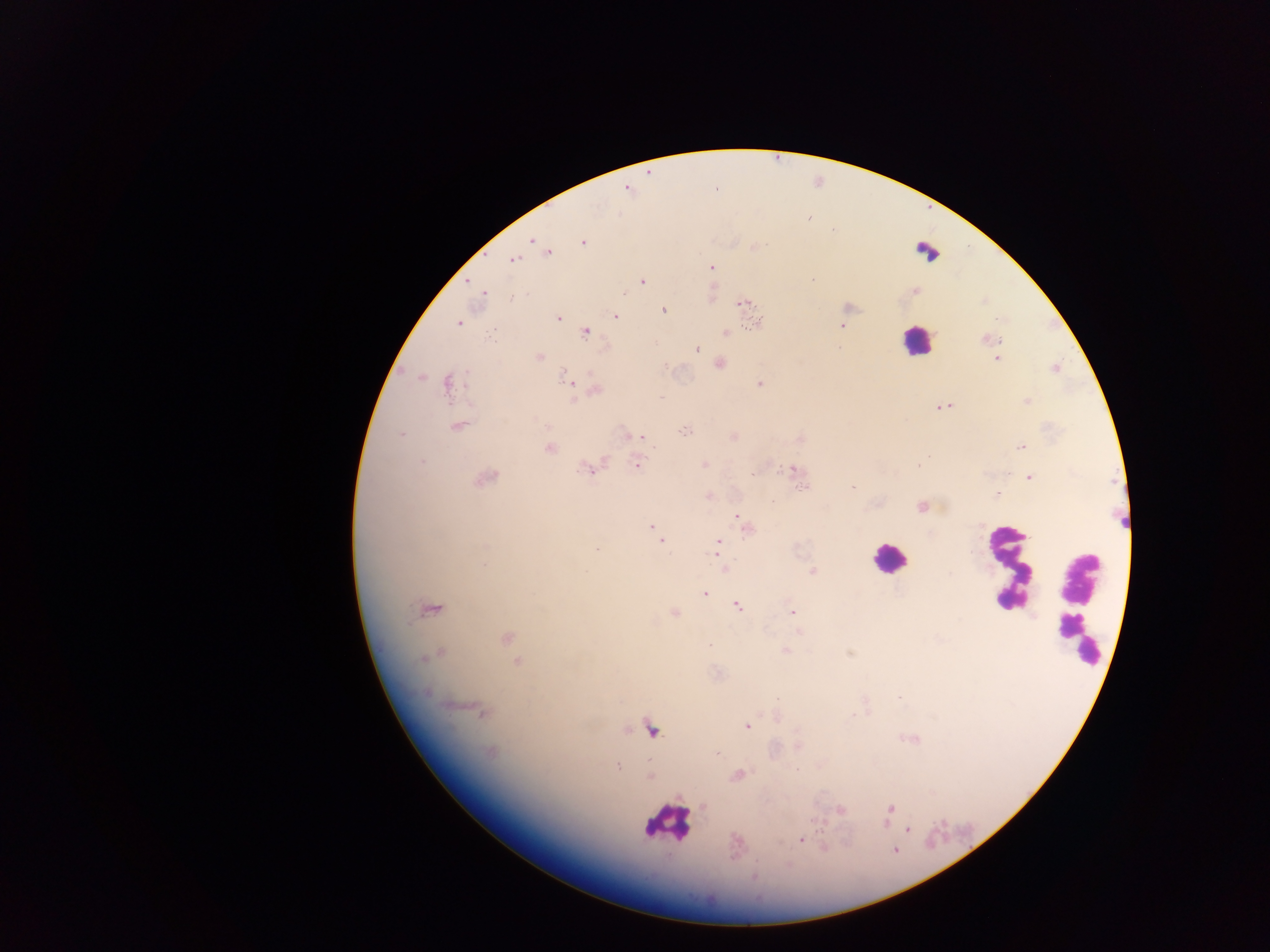

{
  "malaria_parasite_locations": "approximate centers as (x, y) in pixels: (627, 189), (808, 216), (533, 240), (583, 241), (548, 251), (513, 259), (711, 267), (813, 280), (641, 281), (467, 282), (915, 291), (483, 292), (710, 292), (512, 296), (743, 303), (747, 304), (662, 310), (615, 316), (558, 318), (458, 322), (757, 322), (842, 326), (585, 332), (725, 332), (987, 338), (696, 348), (539, 357), (716, 359), (996, 359), (719, 364), (1055, 368), (419, 376), (570, 381), (448, 383), (759, 383), (595, 389), (575, 400), (1027, 401), (942, 406), (458, 425), (684, 430), (402, 433), (732, 436), (637, 437), (799, 438), (550, 447), (1021, 447), (636, 463), (703, 464), (918, 464), (591, 468), (791, 470), (485, 477), (1029, 477), (801, 486), (851, 487), (997, 494), (709, 496), (921, 506), (737, 515), (744, 524), (652, 527), (657, 532), (662, 541), (717, 546), (597, 550), (725, 568), (813, 571), (704, 593), (736, 604), (429, 607), (792, 611), (673, 613), (799, 632), (505, 637), (708, 645), (784, 650), (850, 653), (437, 654), (517, 662), (483, 711), (747, 726), (650, 727), (491, 752), (717, 754), (617, 767), (737, 775), (649, 776), (839, 810), (890, 810), (907, 829), (801, 839), (754, 876)",
  "image_size": "1270×952 pixels",
  "country": "Ghana",
  "preparation": "thick blood film",
  "field_of_view": "single",
  "capture": "mobile-phone photograph through a microscope",
  "leukocyte_locations": "approximate centers as (x, y) in pixels: (926, 252), (917, 342), (888, 559), (1009, 568), (1078, 610), (666, 821)"
}